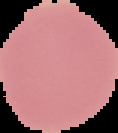 From a thin blood film. Image is 118×133 pixels. The area outside the segmented cell region is set to black. Result: no malaria parasites detected.